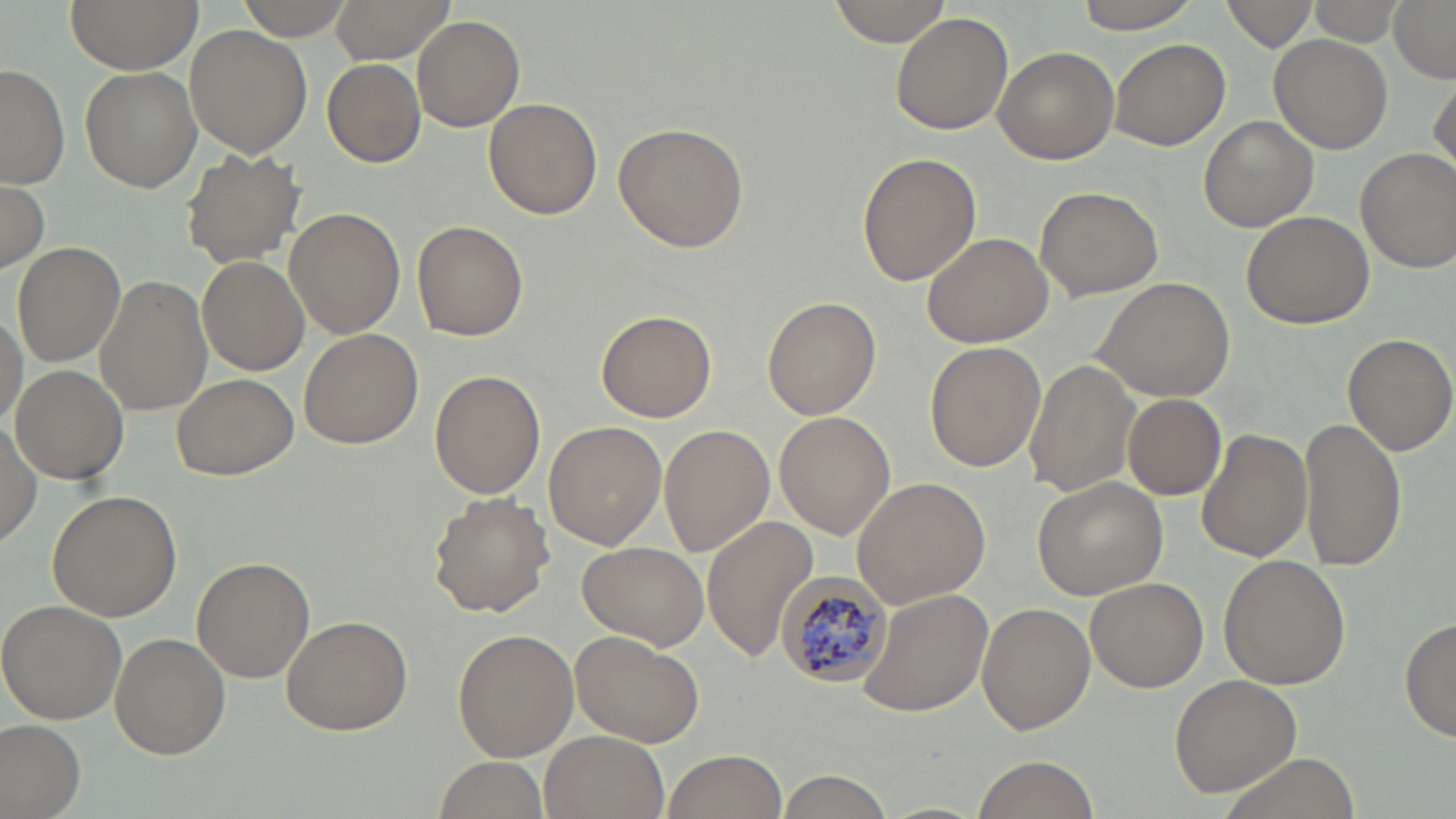

Summary:
  - Coordinate format: approximate bounding boxes as (x1,y1)-(x2,y2) corner pairs in pixels
  - Uninfected red blood cell locations: (68,0)-(198,73), (238,0)-(353,41), (330,0)-(456,65), (827,0)-(954,46), (1075,0)-(1202,33), (1224,0)-(1318,52), (1308,0)-(1403,46), (1385,0)-(1456,81), (890,14)-(1014,136), (412,18)-(524,131), (184,25)-(311,158), (1270,34)-(1392,153), (1110,37)-(1230,150), (993,46)-(1119,165), (321,57)-(425,168), (0,64)-(70,189), (80,66)-(201,193), (1430,75)-(1455,181), (484,97)-(603,220), (1199,115)-(1318,232), (612,122)-(749,253), (179,147)-(305,270), (1356,147)-(1456,272), (857,152)-(981,285), (1,182)-(47,274), (1034,185)-(1164,300), (284,206)-(402,338), (1239,210)-(1374,329), (412,219)-(527,341), (922,231)-(1053,349), (11,241)-(126,367), (197,255)-(310,375), (95,276)-(212,417), (1091,277)-(1236,402), (762,296)-(882,419), (0,300)-(27,436), (596,308)-(716,422), (298,327)-(423,449), (1342,332)-(1455,459), (924,341)-(1046,473), (1026,357)-(1142,498), (9,364)-(128,483), (429,368)-(545,500), (172,372)-(298,480), (1123,393)-(1226,498), (774,411)-(895,538), (1298,412)-(1406,572), (544,421)-(666,548), (1,422)-(42,545), (659,425)-(774,555), (1197,429)-(1311,562), (1032,476)-(1170,601), (851,477)-(991,608), (46,489)-(183,621), (428,493)-(554,617), (701,516)-(818,660), (577,542)-(709,649), (1218,554)-(1351,690), (192,556)-(314,682), (1085,576)-(1208,692), (859,586)-(992,717), (0,598)-(129,723), (977,602)-(1094,734), (280,614)-(413,736), (1400,615)-(1455,744), (452,629)-(578,761), (110,631)-(230,759), (571,632)-(706,748), (1168,673)-(1301,797), (0,719)-(85,817), (541,730)-(667,818), (661,749)-(789,819), (972,754)-(1102,818), (432,755)-(550,819), (775,770)-(896,818)
  - Plasmodium malariae-infected red blood cell locations: (774,568)-(894,688)
  - Slide-level diagnosis: Plasmodium malariae
  - Modality: light microscopy
  - Magnification: 1000x
  - Preparation: thin blood smear
  - Image size: 1456×819 pixels
  - Field of view: one of a larger specimen
  - Stain: May-Grünwald-Giemsa